Give the location of every parasitized RBC.
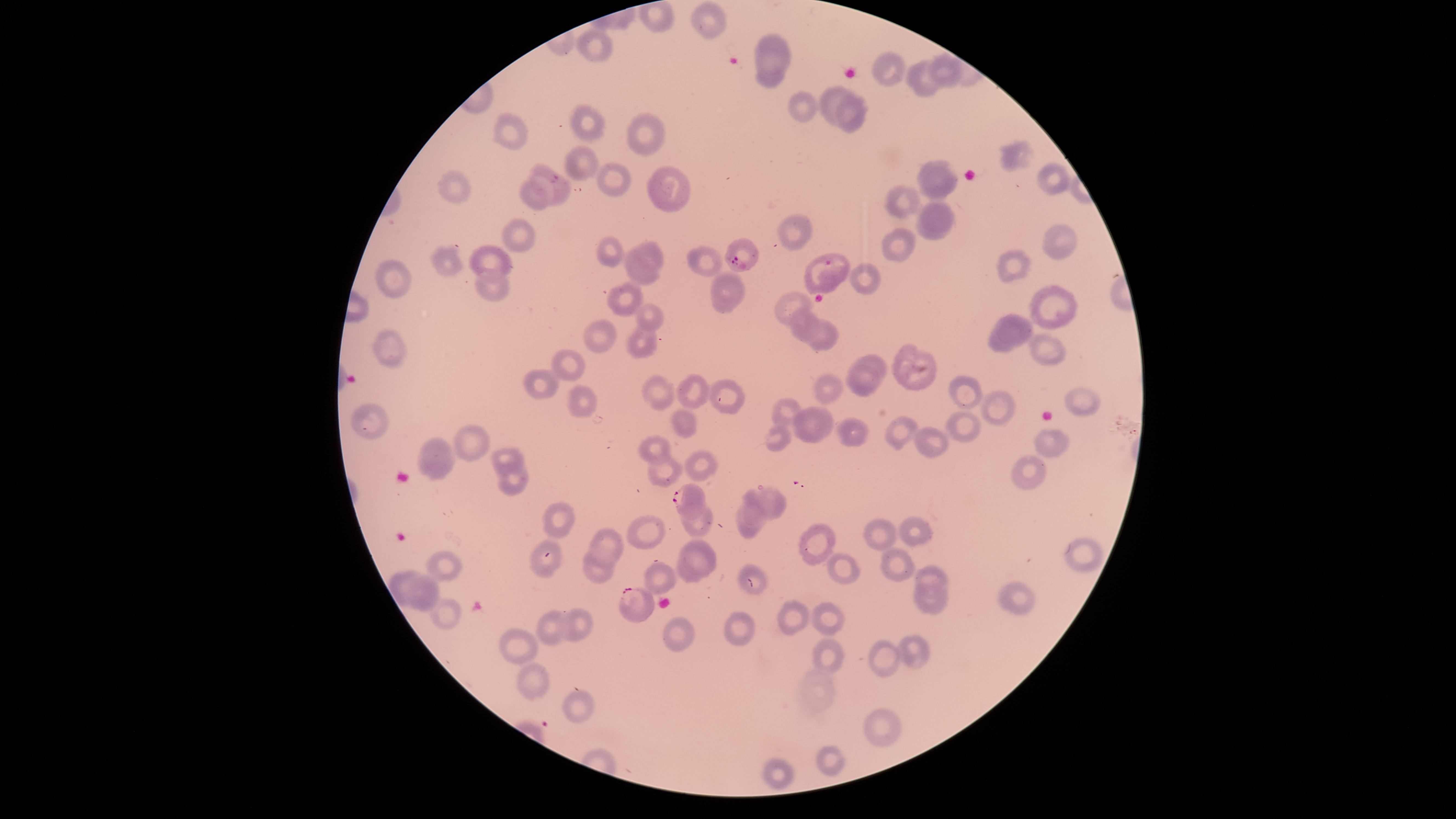
Approximate marker points as {x, y} in pixels.
Parasitized RBCs: {739, 259}, {827, 265}, {687, 496}, {634, 605}.

Approximate marker points as {x, y} in pixels.
Summary:
  - Uninfected RBCs: {698, 20}, {775, 42}, {597, 46}, {893, 67}, {946, 67}, {769, 77}, {927, 79}, {828, 97}, {805, 101}, {858, 116}, {590, 123}, {513, 128}, {644, 130}, {1012, 158}, {580, 165}, {665, 178}, {934, 178}, {1051, 179}, {617, 181}, {449, 183}, {558, 183}, {536, 193}, {896, 198}, {936, 219}, {794, 224}, {514, 233}, {1058, 235}, {893, 246}, {489, 252}, {605, 253}, {651, 254}, {446, 258}, {708, 259}, {1009, 268}, {640, 273}, {868, 277}, {399, 278}, {490, 286}, {733, 293}, {628, 295}, {790, 302}, {1055, 306}, {652, 319}, {799, 328}, {1010, 332}, {606, 337}, {641, 337}, {824, 338}, {387, 347}, {1048, 349}, {566, 362}, {914, 365}, {863, 374}, {546, 383}, {829, 389}, {964, 389}, {693, 391}, {655, 393}, {1079, 396}, {731, 397}, {581, 399}, {997, 404}, {785, 407}, {685, 420}, {375, 422}, {965, 422}, {818, 426}, {904, 429}, {857, 432}, {778, 437}, {931, 439}, {1048, 441}, {474, 446}, {659, 450}, {508, 455}, {439, 456}, {703, 461}, {1026, 468}, {660, 469}, {513, 480}, {765, 500}, {555, 517}, {698, 517}, {751, 519}, {919, 526}, {647, 532}, {880, 534}, {610, 540}, {815, 546}, {1079, 548}, {699, 557}, {891, 564}, {545, 565}, {448, 568}, {842, 569}, {599, 572}, {661, 575}, {930, 577}, {403, 580}, {432, 589}, {1017, 593}, {933, 603}, {446, 609}, {795, 613}, {831, 621}, {578, 624}, {739, 627}, {547, 628}, {681, 632}, {516, 648}, {827, 653}, {917, 653}, {878, 656}, {539, 685}, {577, 707}, {882, 724}, {831, 758}, {780, 771}
  - Species: Plasmodium falciparum
  - Preparation: thin smear of blood
  - Image size: 1456×819 pixels
  - Capture: smartphone photograph through the microscope eyepiece
  - Visible region: circular
  - Field of view: single
  - Stain: Giemsa